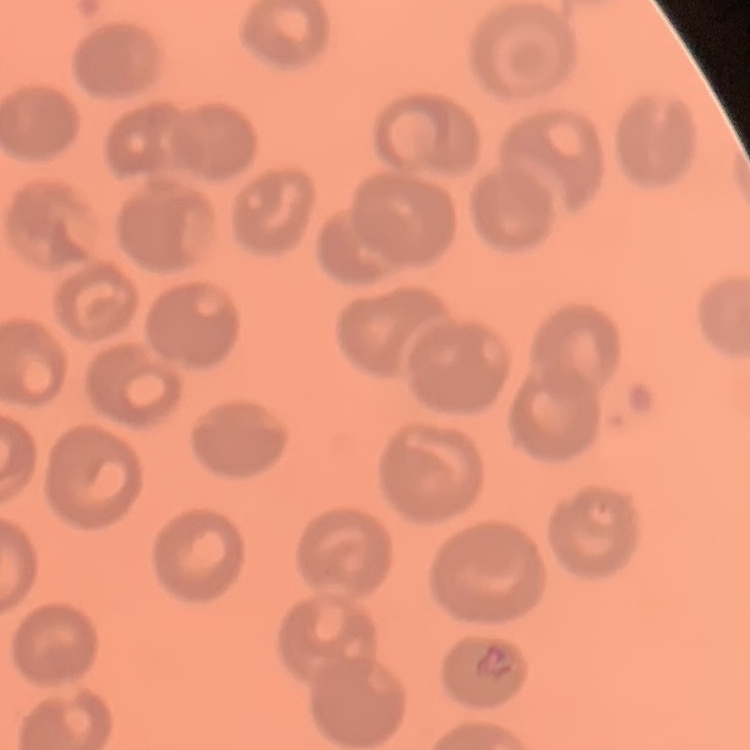

red blood cell morphology = no rouleaux formation
image type = square crop of a larger photomicrograph
stain = Field's or Giemsa
preparation = thin blood film